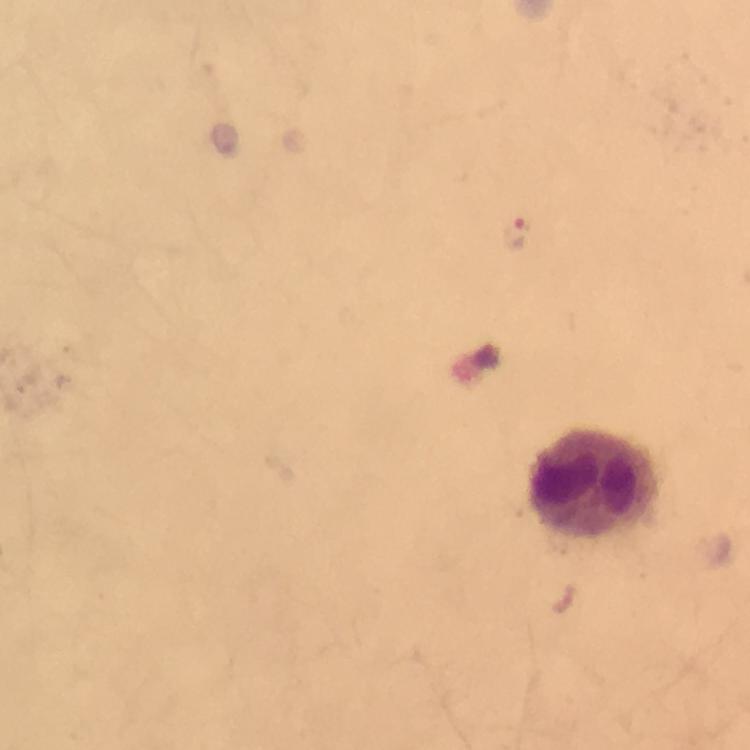 Approximate centers as (x, y) in pixels. Leukocyte locations: (598, 488). Malaria parasite locations: (516, 233). A crop from one field of view. Image is 750×750 pixels. Smartphone photograph taken through a microscope. 100x magnification. Giemsa stain. Thick blood smear. From a diagnostic examination for malaria. Immersion oil applied.